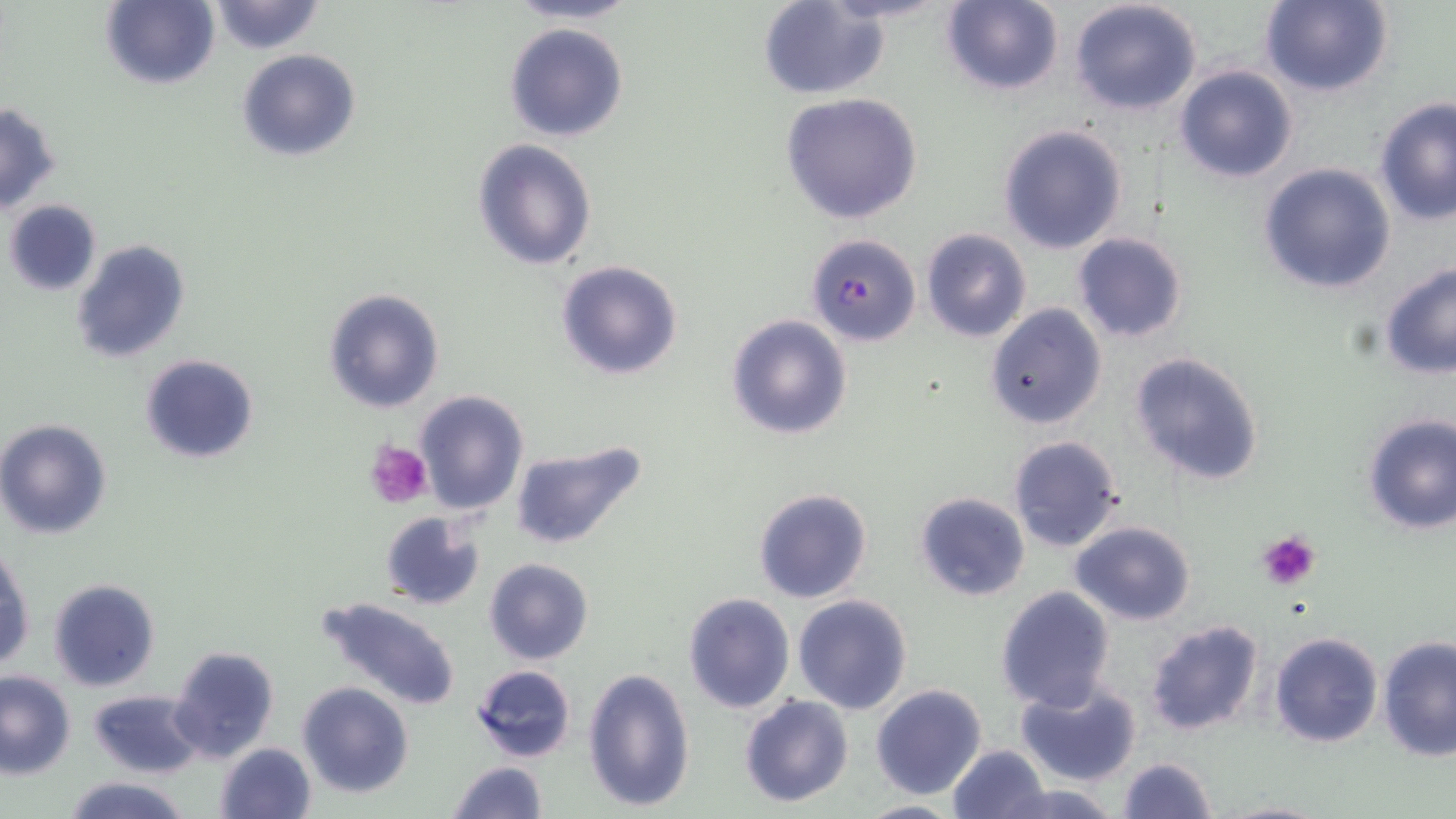
Summary:
  - Coordinate format: approximate bounding boxes as named x1/y1/x2/y2 corners in pixels
  - Plasmodium falciparum-infected red blood cell locations: (x1=805, y1=233, x2=920, y2=347)
  - Platelet locations: (x1=367, y1=440, x2=431, y2=509), (x1=1256, y1=531, x2=1321, y2=591)
  - Uninfected red blood cell locations: (x1=503, y1=0, x2=646, y2=26), (x1=940, y1=0, x2=1065, y2=96), (x1=1068, y1=0, x2=1202, y2=117), (x1=1260, y1=0, x2=1393, y2=98), (x1=98, y1=1, x2=220, y2=90), (x1=206, y1=1, x2=328, y2=54), (x1=757, y1=1, x2=891, y2=98), (x1=504, y1=21, x2=628, y2=142), (x1=237, y1=49, x2=361, y2=161), (x1=1173, y1=65, x2=1299, y2=184), (x1=781, y1=92, x2=923, y2=227), (x1=1374, y1=98, x2=1456, y2=225), (x1=0, y1=104, x2=61, y2=212), (x1=998, y1=123, x2=1129, y2=254), (x1=471, y1=139, x2=598, y2=270), (x1=1257, y1=162, x2=1396, y2=295), (x1=4, y1=199, x2=102, y2=295), (x1=921, y1=229, x2=1033, y2=343), (x1=1072, y1=233, x2=1188, y2=344), (x1=70, y1=238, x2=191, y2=364), (x1=554, y1=259, x2=684, y2=380), (x1=1379, y1=265, x2=1456, y2=380), (x1=323, y1=286, x2=447, y2=414), (x1=984, y1=303, x2=1107, y2=431), (x1=726, y1=314, x2=853, y2=441), (x1=1127, y1=350, x2=1266, y2=486), (x1=139, y1=354, x2=259, y2=463), (x1=414, y1=389, x2=527, y2=515), (x1=1360, y1=413, x2=1456, y2=534), (x1=0, y1=419, x2=112, y2=539), (x1=1006, y1=434, x2=1126, y2=553), (x1=509, y1=442, x2=647, y2=551), (x1=753, y1=487, x2=872, y2=604), (x1=913, y1=490, x2=1030, y2=602), (x1=378, y1=511, x2=486, y2=610), (x1=1070, y1=520, x2=1197, y2=624), (x1=1, y1=547, x2=34, y2=673), (x1=484, y1=558, x2=595, y2=666), (x1=47, y1=578, x2=160, y2=692), (x1=994, y1=585, x2=1117, y2=712), (x1=683, y1=592, x2=794, y2=714), (x1=793, y1=594, x2=912, y2=714), (x1=313, y1=596, x2=463, y2=712), (x1=1145, y1=618, x2=1265, y2=737), (x1=1268, y1=632, x2=1382, y2=748), (x1=1377, y1=636, x2=1456, y2=760), (x1=169, y1=646, x2=281, y2=765), (x1=470, y1=664, x2=577, y2=764), (x1=582, y1=666, x2=696, y2=811), (x1=0, y1=669, x2=76, y2=777), (x1=1015, y1=678, x2=1142, y2=787), (x1=297, y1=681, x2=415, y2=800), (x1=870, y1=683, x2=987, y2=800), (x1=88, y1=688, x2=206, y2=778), (x1=739, y1=695, x2=853, y2=807), (x1=214, y1=742, x2=316, y2=819), (x1=946, y1=744, x2=1051, y2=819), (x1=1117, y1=756, x2=1217, y2=819), (x1=446, y1=762, x2=548, y2=819), (x1=61, y1=775, x2=194, y2=819), (x1=996, y1=781, x2=1119, y2=819), (x1=1214, y1=797, x2=1330, y2=819), (x1=854, y1=798, x2=969, y2=819)
  - Slide-level diagnosis: Plasmodium falciparum
  - Modality: optical microscopy
  - Preparation: thin blood film
  - Field of view: single
  - Stain: May-Grünwald-Giemsa
  - Image size: 1456×819 pixels
  - Magnification: 1000x